Outline each white blood cell.
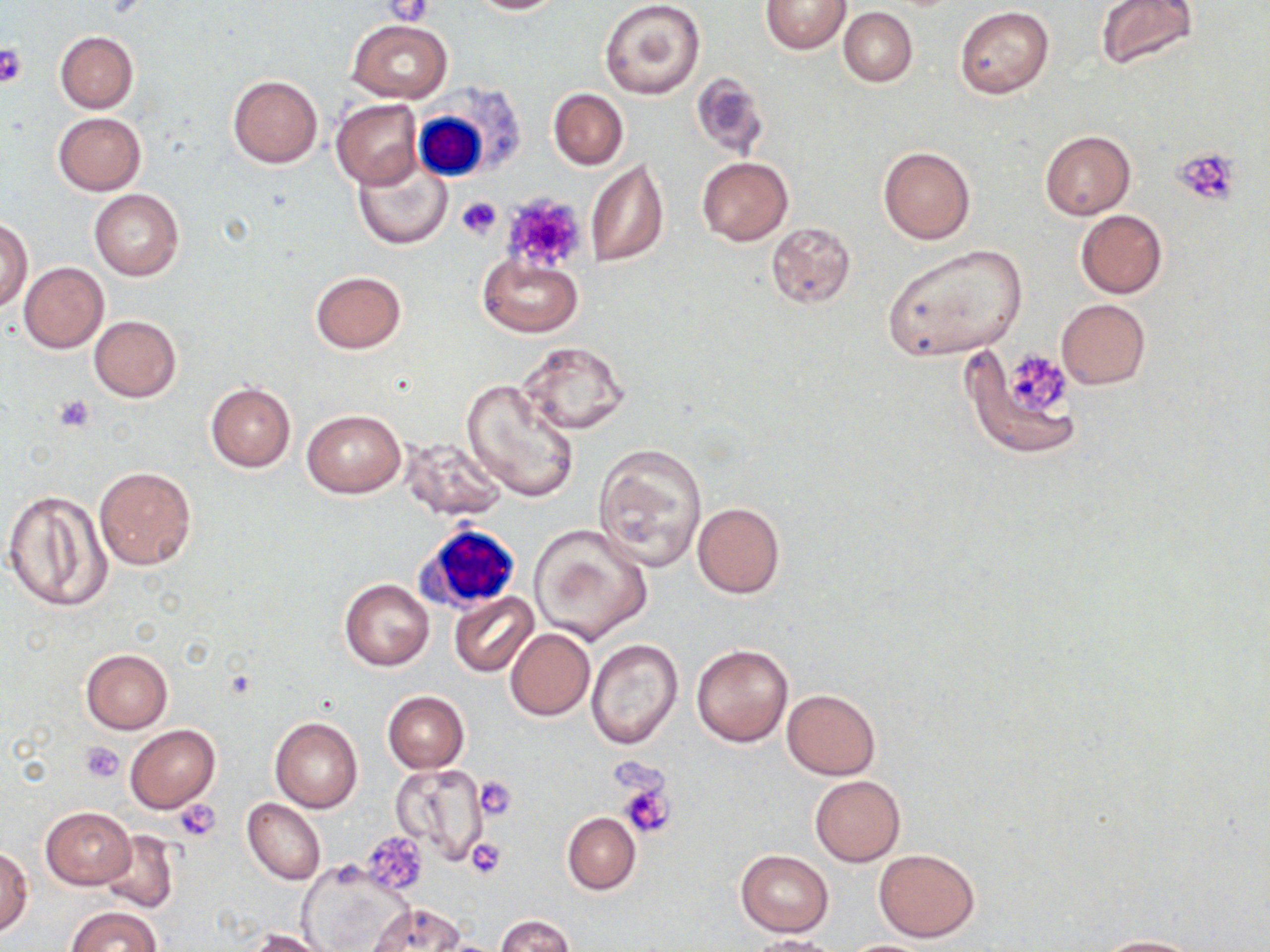
Approximate bounding boxes as named x1/y1/x2/y2 corners in pixels.
White blood cells: (x1=412, y1=99, x2=502, y2=184), (x1=415, y1=523, x2=523, y2=611).

Summary:
  - Uninfected red blood cell locations (subset): (x1=465, y1=0, x2=567, y2=14), (x1=599, y1=0, x2=705, y2=99), (x1=1095, y1=0, x2=1199, y2=70), (x1=761, y1=1, x2=851, y2=54), (x1=955, y1=6, x2=1054, y2=99), (x1=839, y1=7, x2=918, y2=87), (x1=348, y1=19, x2=451, y2=102), (x1=55, y1=31, x2=138, y2=113), (x1=692, y1=73, x2=770, y2=159), (x1=227, y1=75, x2=322, y2=168), (x1=548, y1=88, x2=628, y2=169), (x1=331, y1=99, x2=422, y2=189), (x1=53, y1=112, x2=147, y2=195), (x1=1040, y1=130, x2=1135, y2=219), (x1=879, y1=146, x2=975, y2=245), (x1=353, y1=153, x2=453, y2=251), (x1=696, y1=156, x2=793, y2=246), (x1=585, y1=157, x2=669, y2=268), (x1=89, y1=190, x2=184, y2=280), (x1=1075, y1=210, x2=1168, y2=299), (x1=0, y1=219, x2=32, y2=311), (x1=767, y1=221, x2=857, y2=310), (x1=881, y1=244, x2=1029, y2=361), (x1=477, y1=256, x2=582, y2=337), (x1=19, y1=263, x2=108, y2=353), (x1=310, y1=271, x2=406, y2=354), (x1=1055, y1=300, x2=1151, y2=390), (x1=89, y1=314, x2=181, y2=402), (x1=517, y1=339, x2=632, y2=438), (x1=960, y1=345, x2=1081, y2=458), (x1=462, y1=377, x2=578, y2=501), (x1=206, y1=382, x2=295, y2=472), (x1=301, y1=408, x2=406, y2=499), (x1=400, y1=437, x2=508, y2=522), (x1=592, y1=443, x2=708, y2=573), (x1=94, y1=465, x2=197, y2=571), (x1=1, y1=490, x2=114, y2=613), (x1=691, y1=501, x2=785, y2=599), (x1=529, y1=524, x2=652, y2=646), (x1=339, y1=579, x2=434, y2=671), (x1=449, y1=593, x2=538, y2=677), (x1=505, y1=627, x2=595, y2=721), (x1=585, y1=639, x2=683, y2=748), (x1=691, y1=644, x2=792, y2=746), (x1=81, y1=650, x2=173, y2=733), (x1=782, y1=689, x2=881, y2=780), (x1=383, y1=691, x2=469, y2=772), (x1=270, y1=716, x2=363, y2=813), (x1=126, y1=724, x2=219, y2=812), (x1=393, y1=761, x2=493, y2=865), (x1=810, y1=776, x2=905, y2=866), (x1=243, y1=798, x2=326, y2=885), (x1=40, y1=806, x2=137, y2=888), (x1=562, y1=813, x2=640, y2=894), (x1=97, y1=830, x2=179, y2=914), (x1=873, y1=847, x2=980, y2=942), (x1=0, y1=848, x2=32, y2=934), (x1=737, y1=850, x2=833, y2=936), (x1=300, y1=864, x2=408, y2=951), (x1=366, y1=903, x2=466, y2=951), (x1=66, y1=905, x2=161, y2=952), (x1=496, y1=916, x2=574, y2=952), (x1=251, y1=929, x2=333, y2=952), (x1=749, y1=936, x2=844, y2=952), (x1=1088, y1=936, x2=1210, y2=952), (x1=838, y1=939, x2=938, y2=952)
  - Platelet locations (subset): (x1=380, y1=1, x2=432, y2=26), (x1=0, y1=44, x2=28, y2=89), (x1=1170, y1=147, x2=1243, y2=206), (x1=506, y1=194, x2=588, y2=271), (x1=457, y1=196, x2=501, y2=239), (x1=1010, y1=354, x2=1072, y2=412), (x1=55, y1=394, x2=96, y2=433), (x1=80, y1=741, x2=124, y2=783), (x1=476, y1=777, x2=518, y2=821), (x1=619, y1=781, x2=674, y2=838), (x1=175, y1=798, x2=222, y2=842), (x1=467, y1=839, x2=505, y2=877)
  - Slide-level diagnosis: negative for blood parasites
  - Stain: May-Grünwald-Giemsa
  - Preparation: thin blood smear
  - Image size: 1270×952 pixels
  - Magnification: 1000x
  - Modality: light microscopy
  - Field of view: single